Locate every blood parasite and identify its species.
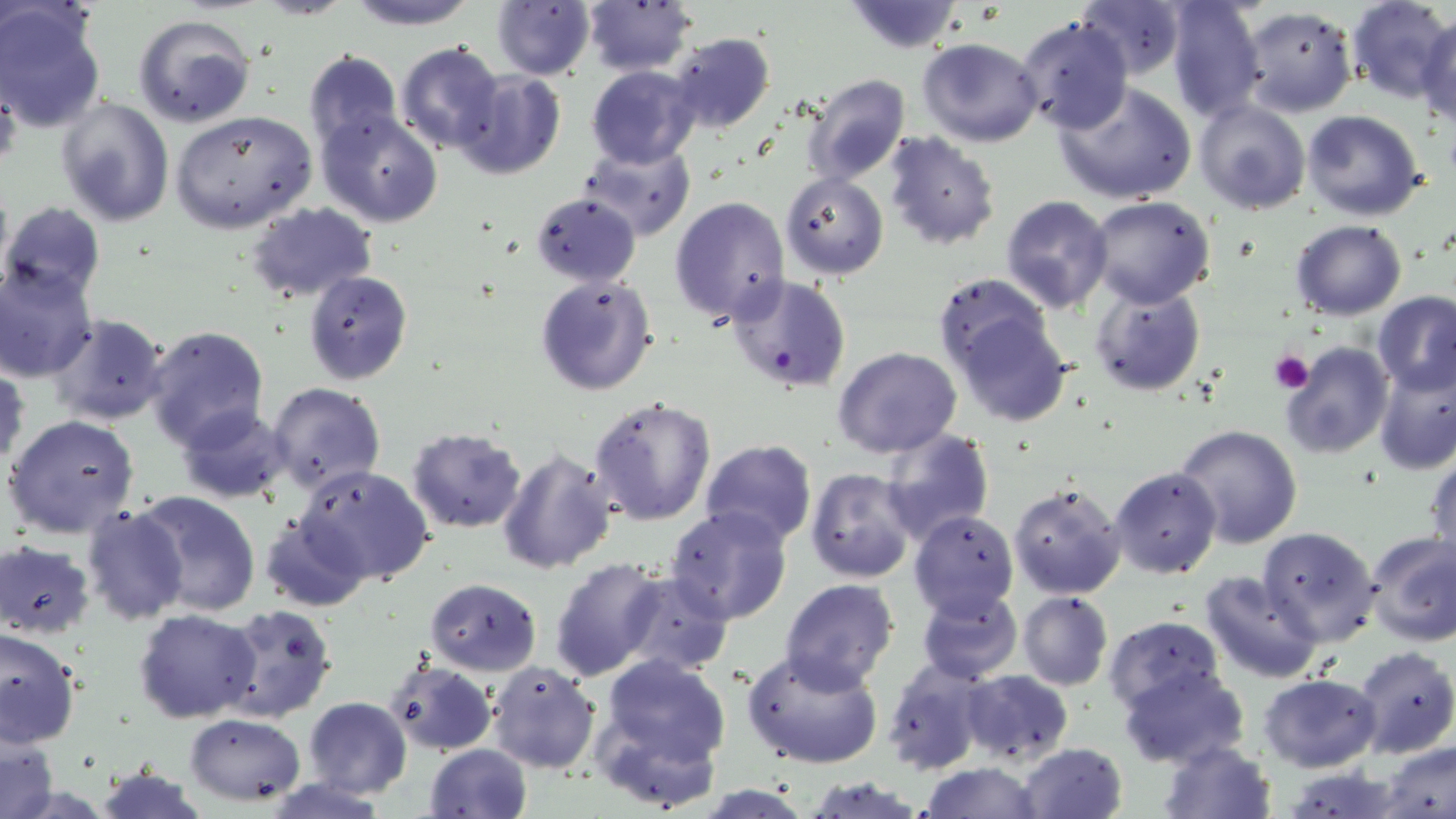

Approximate bounding boxes as [x1, y1, x2, y2] in pixels.
Plasmodium falciparum-infected red blood cells: [727, 274, 852, 393].
No Plasmodium ovale, Plasmodium malariae, Plasmodium vivax, Babesia divergens, or Trypanosoma brucei observed.

Summary:
  - Platelet locations: [1271, 348, 1314, 393]
  - Uninfected red blood cell locations: [342, 0, 479, 30], [490, 0, 596, 81], [582, 0, 697, 74], [1165, 0, 1267, 123], [1346, 0, 1455, 103], [845, 1, 966, 52], [1077, 1, 1187, 81], [0, 3, 107, 131], [1239, 5, 1356, 117], [1417, 10, 1456, 127], [133, 13, 257, 129], [1014, 15, 1134, 136], [667, 34, 776, 136], [1025, 37, 1170, 180], [916, 39, 1042, 148], [395, 42, 506, 155], [301, 49, 403, 154], [587, 64, 702, 168], [453, 69, 566, 180], [800, 73, 912, 187], [1053, 81, 1197, 205], [55, 97, 175, 226], [1193, 99, 1311, 214], [316, 108, 442, 229], [170, 109, 317, 232], [1302, 109, 1425, 221], [882, 130, 1000, 252], [580, 143, 695, 239], [779, 172, 889, 278], [530, 192, 641, 287], [669, 195, 791, 324], [1001, 195, 1114, 314], [1087, 197, 1216, 309], [0, 201, 105, 305], [246, 201, 380, 306], [1290, 220, 1407, 320], [0, 264, 98, 381], [303, 270, 412, 385], [933, 273, 1054, 380], [534, 275, 657, 395], [1089, 283, 1207, 397], [1372, 292, 1456, 396], [949, 305, 1072, 426], [45, 313, 171, 427], [143, 324, 269, 449], [1280, 341, 1394, 460], [833, 347, 962, 459], [1, 361, 28, 478], [1374, 365, 1456, 475], [267, 383, 387, 497], [587, 393, 717, 525], [176, 403, 291, 505], [4, 414, 138, 540], [1174, 424, 1305, 549], [406, 427, 526, 532], [879, 427, 995, 545], [700, 440, 816, 548], [496, 449, 618, 575], [1427, 451, 1455, 568], [295, 464, 434, 586], [1109, 466, 1223, 578], [806, 468, 917, 583], [1008, 480, 1126, 600], [131, 490, 261, 618], [81, 505, 188, 624], [665, 506, 794, 625], [909, 510, 1019, 621], [260, 511, 371, 613], [1259, 525, 1380, 645], [1364, 530, 1456, 647], [0, 540, 97, 638], [549, 558, 670, 681], [616, 570, 735, 678], [1198, 570, 1324, 684], [425, 579, 542, 675], [779, 580, 899, 694], [916, 584, 1024, 684], [1017, 591, 1113, 690], [1014, 600, 1217, 697], [215, 603, 337, 723], [134, 609, 261, 722], [1105, 616, 1224, 712], [1, 628, 80, 750], [1352, 646, 1456, 759], [741, 648, 884, 770], [597, 653, 732, 773], [384, 658, 499, 755], [884, 659, 991, 777], [486, 660, 601, 775], [1119, 667, 1250, 769], [958, 669, 1073, 765], [1260, 674, 1381, 771], [304, 696, 411, 797], [185, 714, 307, 803], [0, 735, 58, 819], [1157, 739, 1275, 819], [1378, 740, 1455, 819], [1014, 741, 1127, 819], [423, 743, 534, 819], [917, 762, 1045, 818], [91, 763, 211, 819], [807, 775, 925, 818]
  - Slide-level diagnosis: Plasmodium falciparum
  - Magnification: 1000x
  - Image size: 1456×819 pixels
  - Stain: May-Grünwald-Giemsa
  - Modality: light microscopy
  - Preparation: thin blood film
  - Field of view: single